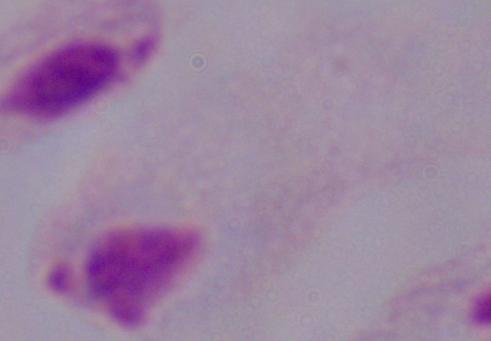

Photomicrograph. A trichomonad is shown. Captured at 1000x magnification.